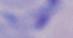

{
  "modality": "photomicrograph",
  "identification": "trypanosome",
  "magnification": "1000x"
}